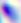
Summary:
  - Magnification: 400x
  - Identification: Toxoplasma gondii
  - Modality: photomicrograph